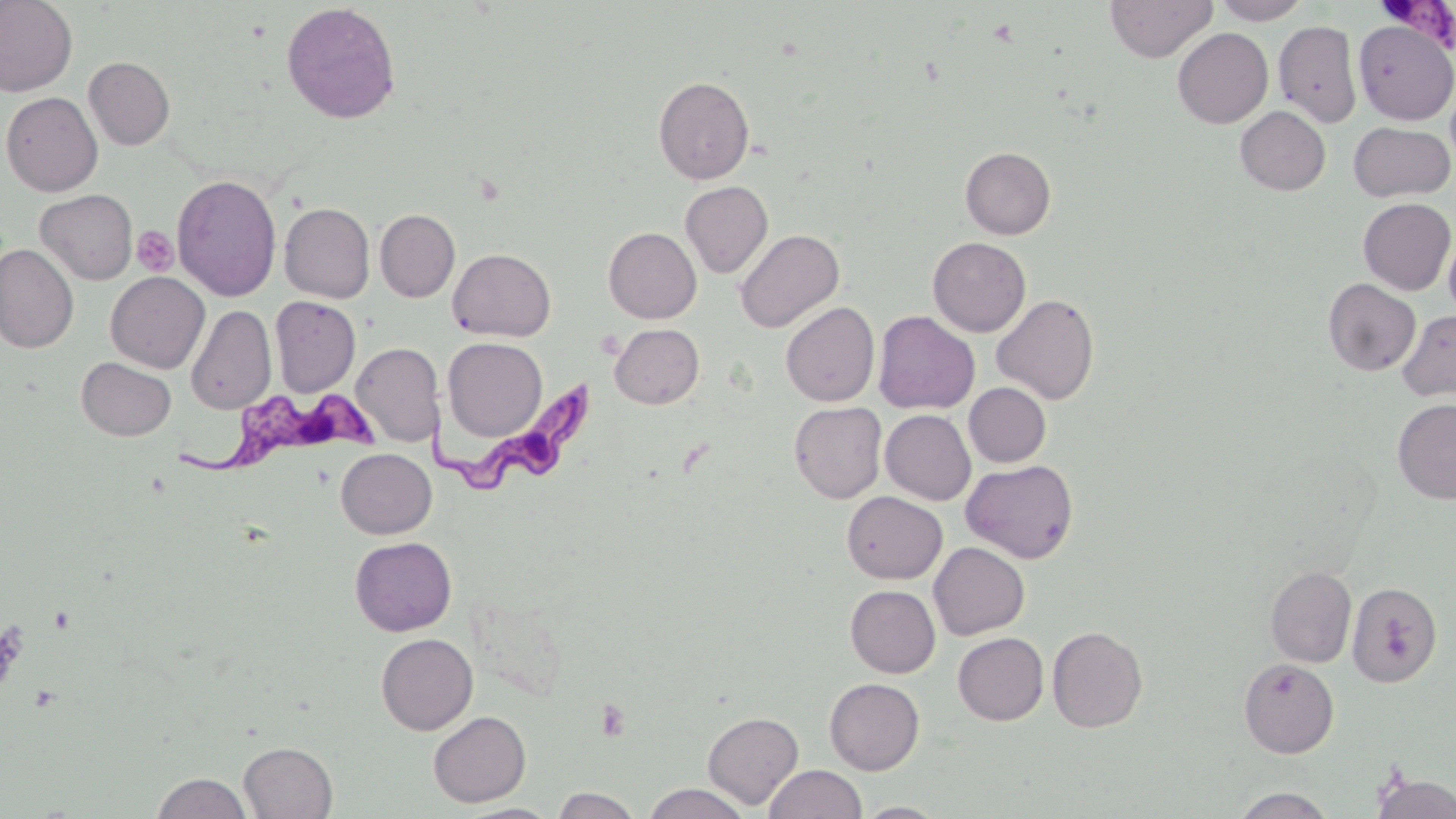
Approximate bounding boxes as [x1, y1, x2, y2] in pixels. Trypanosoma brucei locations: [1375, 5, 1455, 57], [426, 379, 599, 491], [178, 383, 377, 485]. Platelet locations: [132, 226, 178, 277], [596, 698, 631, 741]. Uninfected red blood cell locations: [0, 0, 77, 97], [1105, 0, 1217, 62], [1211, 0, 1313, 24], [280, 3, 402, 124], [1274, 20, 1362, 127], [1354, 20, 1456, 124], [1172, 28, 1273, 128], [84, 57, 175, 150], [653, 76, 754, 184], [1445, 78, 1456, 171], [1, 91, 103, 196], [1235, 106, 1331, 195], [1348, 122, 1455, 202], [960, 147, 1056, 239], [172, 174, 282, 302], [680, 181, 773, 278], [35, 189, 137, 284], [1358, 198, 1455, 294], [279, 202, 375, 303], [375, 209, 460, 302], [603, 227, 701, 323], [1443, 227, 1456, 325], [735, 229, 844, 332], [928, 236, 1031, 337], [0, 244, 78, 353], [448, 248, 556, 341], [106, 271, 209, 373], [1323, 278, 1421, 376], [992, 294, 1100, 404], [270, 296, 360, 396], [781, 301, 879, 406], [186, 305, 276, 414], [1397, 309, 1456, 401], [873, 311, 979, 414], [610, 324, 704, 409], [443, 337, 547, 441], [350, 342, 443, 447], [76, 357, 176, 441], [964, 382, 1051, 467], [1392, 398, 1456, 504], [789, 401, 887, 503], [880, 409, 975, 505], [336, 448, 436, 538], [960, 459, 1079, 564], [842, 491, 947, 583], [350, 536, 457, 636], [929, 542, 1029, 640], [1265, 567, 1356, 668], [1346, 581, 1442, 687], [846, 585, 940, 678], [1047, 626, 1148, 732], [953, 632, 1048, 725], [376, 633, 478, 734], [1238, 658, 1339, 758], [824, 678, 924, 775], [428, 710, 530, 807], [702, 711, 803, 809], [238, 741, 338, 819], [764, 764, 866, 819], [151, 772, 253, 818], [1370, 773, 1456, 819], [642, 783, 751, 819], [1230, 786, 1336, 818], [552, 788, 642, 818], [856, 802, 948, 818], [452, 803, 562, 819]. Slide-level diagnosis: Trypanosoma brucei. Single field of view. Captured at 1000x magnification. Image is 1456×819 pixels. Thin blood smear. Light microscopy. May-Grünwald-Giemsa-stained preparation.